Identify the preparation type.
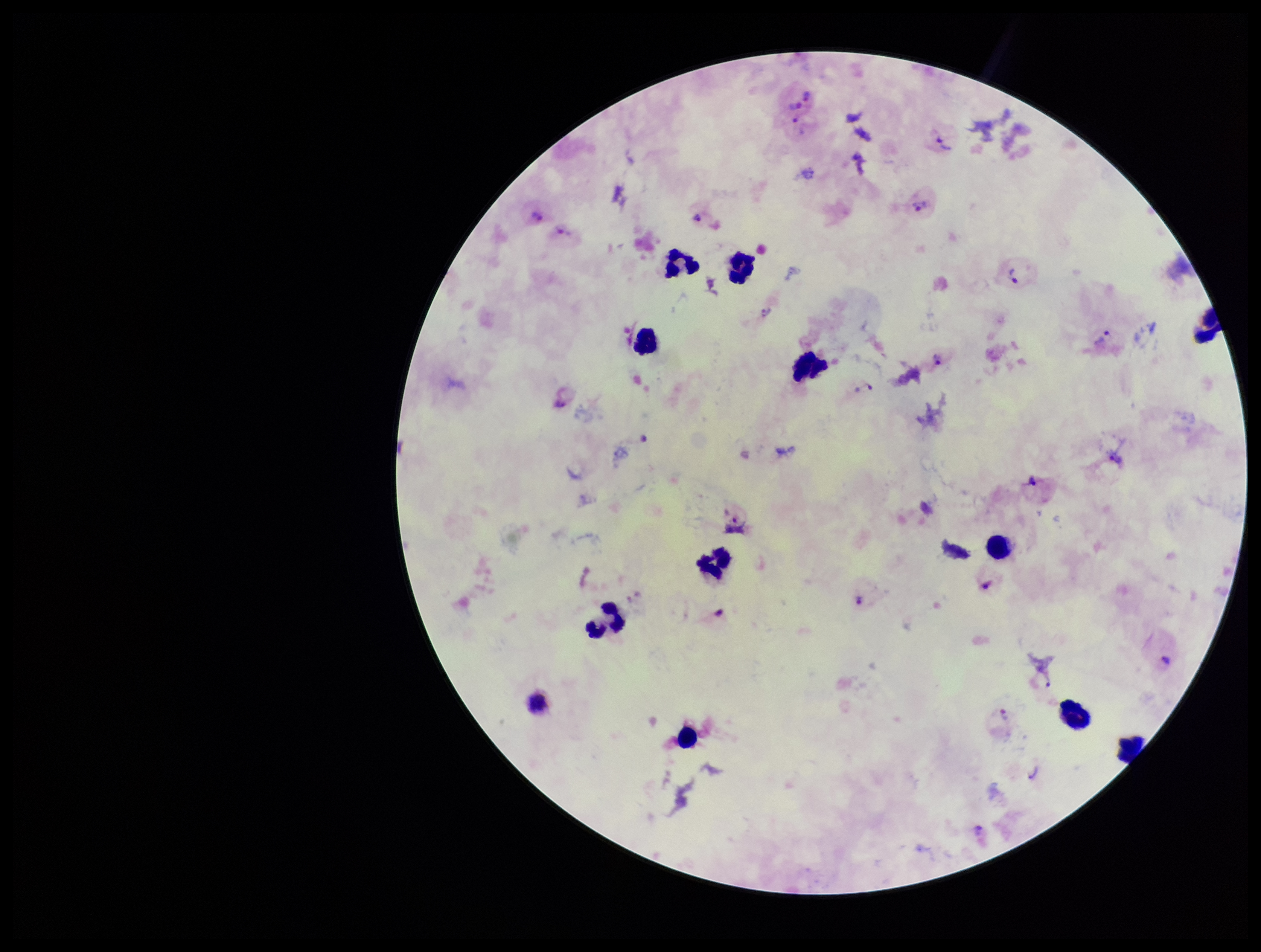

A thick smear.

One field from this slide. Image is 1261×952 pixels. Species reported for this patient: Plasmodium vivax. Smartphone photograph taken through the eyepiece of a microscope. Plasmodium parasites: seen. Giemsa stain. Parasite count: 19. Leukocyte count: 12. Patient malaria status: infected.